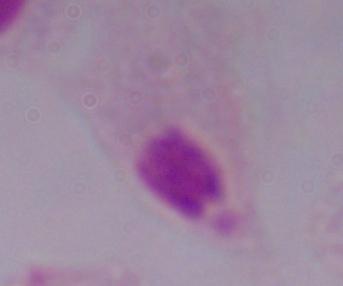
modality = micrograph
magnification = 1000x
identification = trichomonad